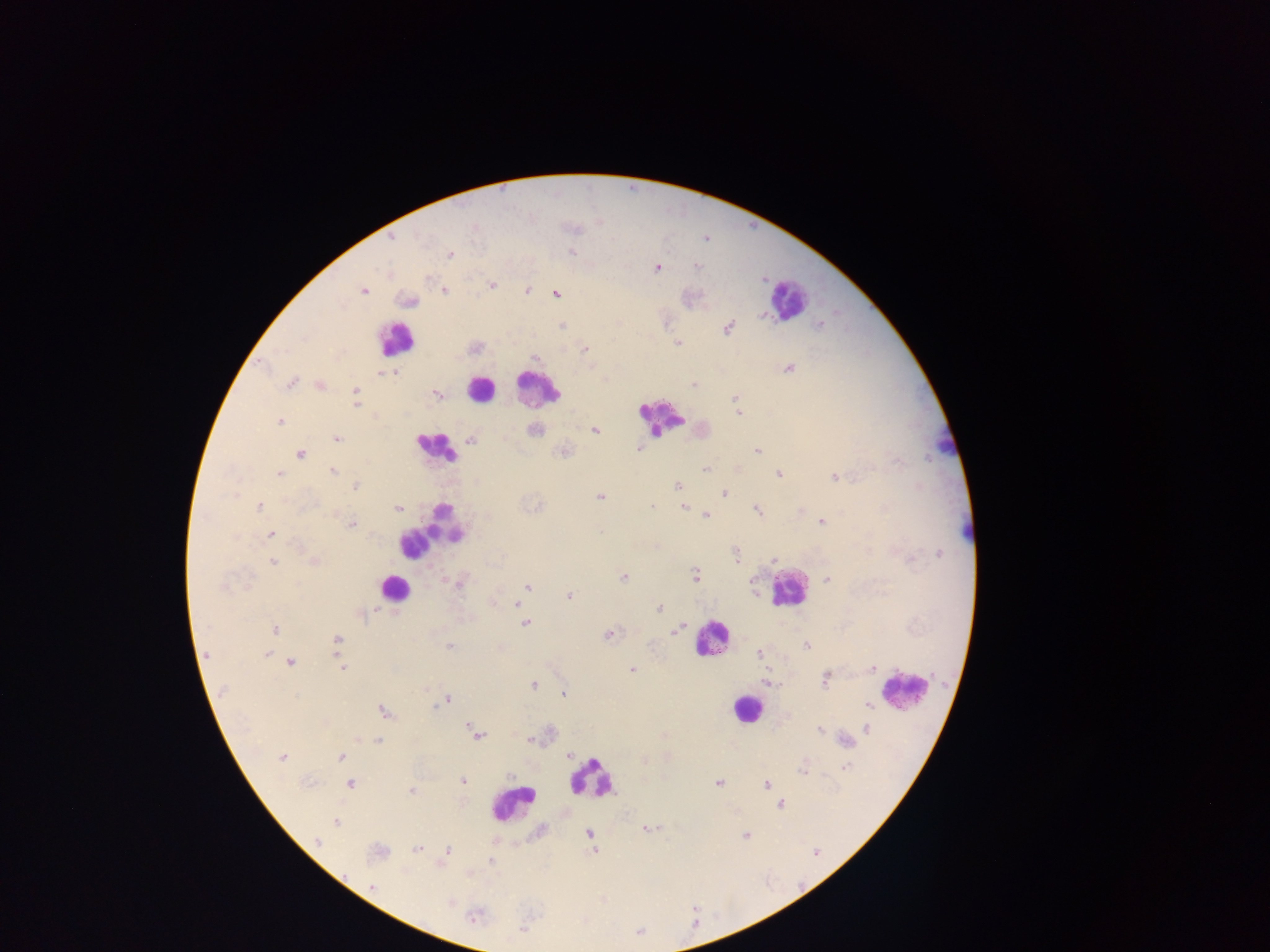
{
  "malaria_parasite_locations": "approximate centers as {x, y} in pixels: {391, 237}, {449, 254}, {695, 266}, {656, 267}, {491, 284}, {363, 290}, {443, 290}, {527, 290}, {556, 294}, {409, 301}, {819, 325}, {562, 326}, {727, 328}, {678, 342}, {585, 349}, {789, 368}, {394, 372}, {290, 382}, {319, 384}, {693, 385}, {355, 391}, {436, 394}, {735, 398}, {355, 404}, {739, 413}, {279, 421}, {534, 430}, {594, 430}, {336, 439}, {470, 439}, {644, 449}, {638, 450}, {757, 450}, {564, 451}, {300, 453}, {736, 469}, {705, 470}, {333, 471}, {779, 473}, {278, 474}, {835, 477}, {354, 486}, {677, 486}, {724, 494}, {599, 496}, {652, 505}, {257, 506}, {684, 506}, {397, 508}, {756, 509}, {706, 514}, {821, 521}, {351, 525}, {271, 534}, {939, 554}, {735, 557}, {773, 558}, {312, 560}, {273, 561}, {695, 575}, {623, 577}, {826, 579}, {459, 581}, {528, 586}, {567, 596}, {518, 603}, {660, 608}, {360, 613}, {525, 622}, {678, 625}, {273, 629}, {676, 630}, {609, 635}, {336, 641}, {805, 645}, {448, 646}, {267, 653}, {758, 653}, {205, 655}, {289, 662}, {343, 668}, {871, 668}, {631, 670}, {825, 677}, {768, 683}, {533, 685}, {563, 694}, {867, 699}, {446, 700}, {866, 704}, {382, 712}, {469, 726}, {867, 728}, {820, 729}, {477, 735}, {530, 739}, {377, 740}, {844, 741}, {568, 755}, {342, 757}, {281, 758}, {846, 767}, {803, 771}, {462, 781}, {350, 783}, {717, 783}, {765, 784}, {411, 789}, {779, 803}, {335, 822}, {647, 829}, {589, 834}, {745, 835}, {592, 841}, {317, 843}, {417, 849}, {447, 850}, {377, 851}, {594, 851}, {489, 861}, {371, 887}, {448, 900}, {473, 916}",
  "country": "Ghana",
  "preparation": "thick blood smear",
  "field_of_view": "single",
  "image_size": "1270×952 pixels",
  "capture": "mobile-phone photograph through a microscope",
  "leukocyte_locations": "approximate centers as {x, y} in pixels: {787, 299}, {394, 339}, {482, 388}, {536, 389}, {662, 416}, {944, 442}, {434, 447}, {431, 527}, {965, 533}, {394, 588}, {788, 589}, {711, 637}, {903, 690}, {748, 710}, {591, 778}, {512, 803}"
}